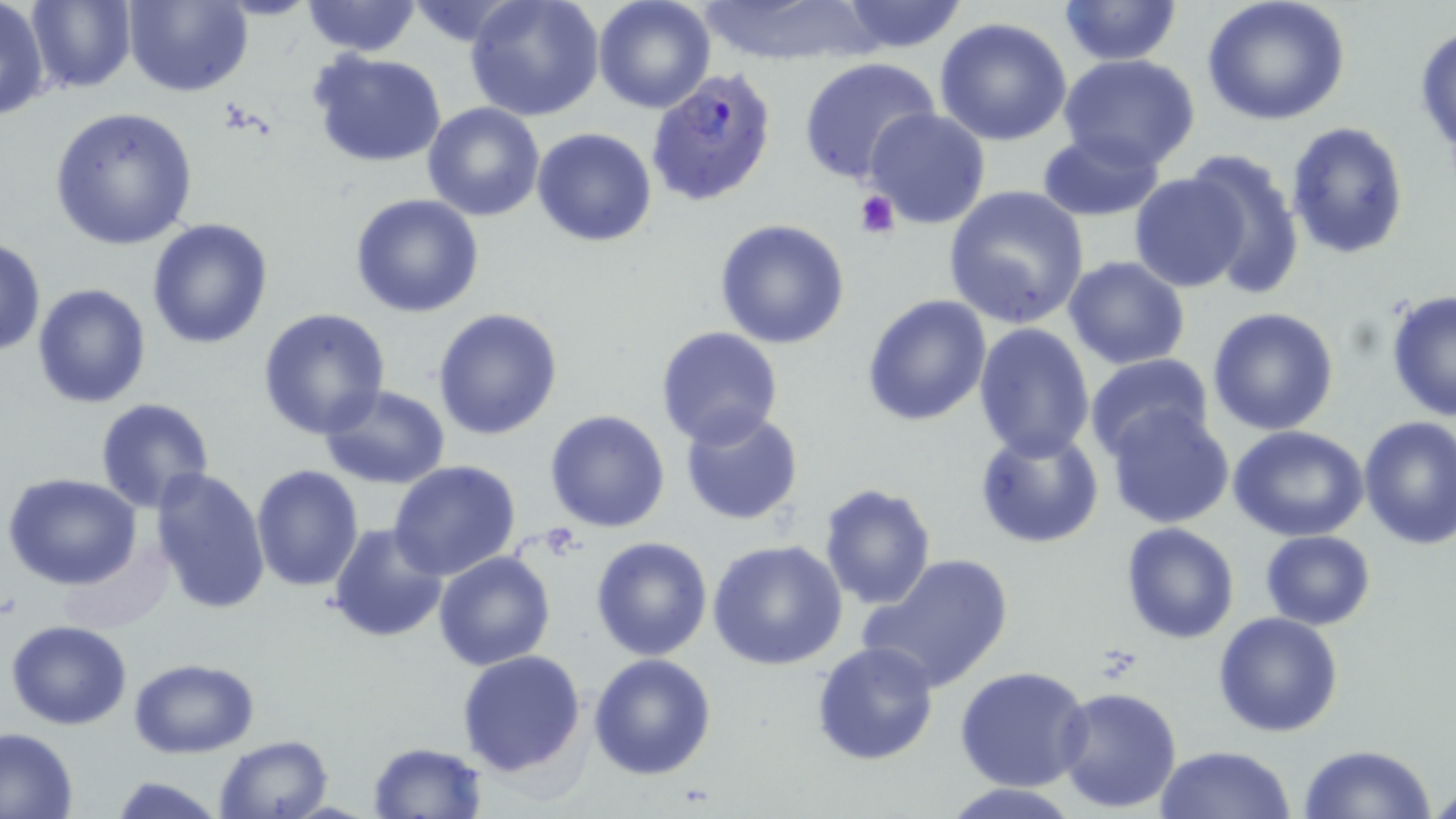
slide-level diagnosis = Plasmodium falciparum
preparation = thin blood film
platelet locations = approximate bounding boxes as (x1, y1, x2, y2) in pixels: (855, 188, 901, 239)
stain = May-Grünwald-Giemsa
image size = 1456×819 pixels
Plasmodium falciparum-infected red blood cell locations = approximate bounding boxes as (x1, y1, x2, y2) in pixels: (645, 71, 777, 205)
uninfected red blood cell locations = approximate bounding boxes as (x1, y1, x2, y2) in pixels: (26, 0, 137, 92), (122, 0, 253, 96), (465, 0, 604, 122), (693, 0, 878, 67), (1200, 0, 1352, 126), (0, 1, 51, 122), (301, 1, 422, 56), (403, 1, 523, 44), (592, 1, 716, 114), (834, 1, 971, 53), (1057, 1, 1184, 67), (933, 17, 1073, 146), (1413, 23, 1456, 165), (310, 49, 448, 167), (1058, 54, 1203, 171), (797, 57, 942, 186), (423, 101, 544, 221), (50, 106, 196, 251), (864, 108, 991, 229), (1286, 122, 1409, 260), (532, 127, 656, 246), (1036, 131, 1166, 221), (1182, 150, 1305, 300), (1129, 171, 1248, 292), (944, 186, 1091, 330), (350, 194, 485, 318), (713, 218, 850, 349), (147, 219, 274, 351), (0, 236, 46, 357), (1062, 257, 1190, 370), (32, 282, 153, 408), (1385, 290, 1455, 423), (862, 293, 992, 428), (1207, 306, 1341, 436), (257, 307, 391, 441), (432, 307, 563, 440), (972, 323, 1095, 462), (655, 325, 784, 447), (1084, 353, 1215, 461), (317, 383, 450, 489), (95, 398, 216, 514), (1105, 404, 1235, 527), (679, 409, 804, 526), (544, 410, 672, 533), (1357, 416, 1456, 549), (973, 424, 1105, 548), (1227, 425, 1371, 542), (387, 460, 522, 580), (249, 464, 363, 593), (150, 467, 270, 615), (4, 474, 143, 589), (819, 482, 937, 609), (1120, 523, 1239, 643), (325, 524, 448, 643), (1261, 529, 1376, 629), (589, 536, 713, 660), (708, 539, 846, 670), (433, 551, 555, 672), (855, 552, 1014, 693), (1214, 611, 1344, 738), (5, 620, 132, 730), (810, 640, 938, 766), (457, 649, 586, 778), (587, 652, 716, 779), (128, 657, 258, 758), (955, 666, 1095, 792), (1055, 685, 1185, 814), (0, 727, 78, 818), (214, 735, 333, 818), (369, 742, 486, 817), (1155, 743, 1296, 819), (1300, 745, 1435, 819), (110, 775, 226, 818), (1430, 780, 1456, 816), (941, 781, 1077, 817)
modality = light microscopy
field of view = one of a larger specimen
magnification = 1000x